Assess the morphology of the red blood cells.
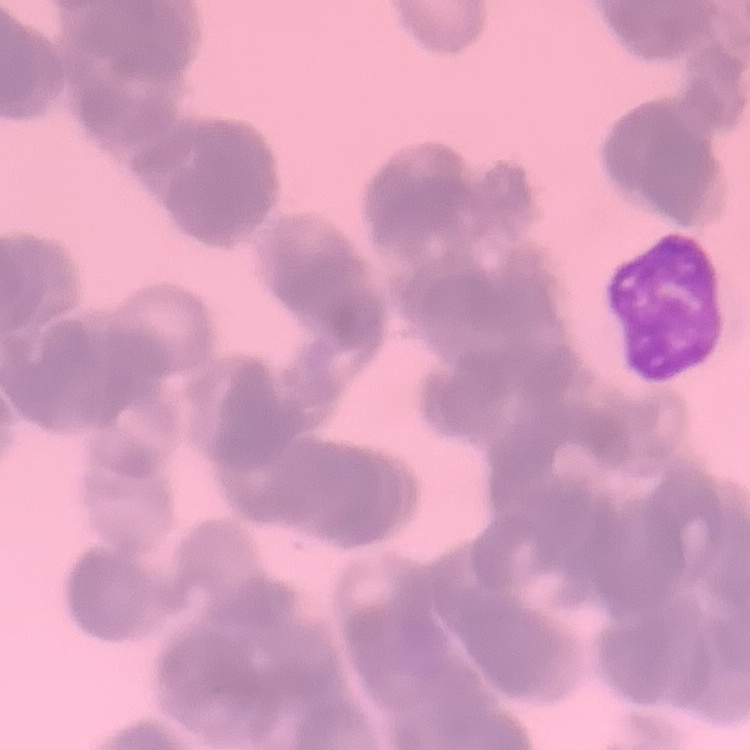
They show rouleaux formation.

Summary:
  - Stain: Field's or Giemsa
  - Preparation: thin peripheral smear
  - Image type: one tile cut from a larger photomicrograph